Classify this cell by malaria status.
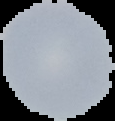
Uninfected.

preparation = thin blood film
image size = 115×121 pixels
image type = segmented cell region on a black background